Assess for malaria.
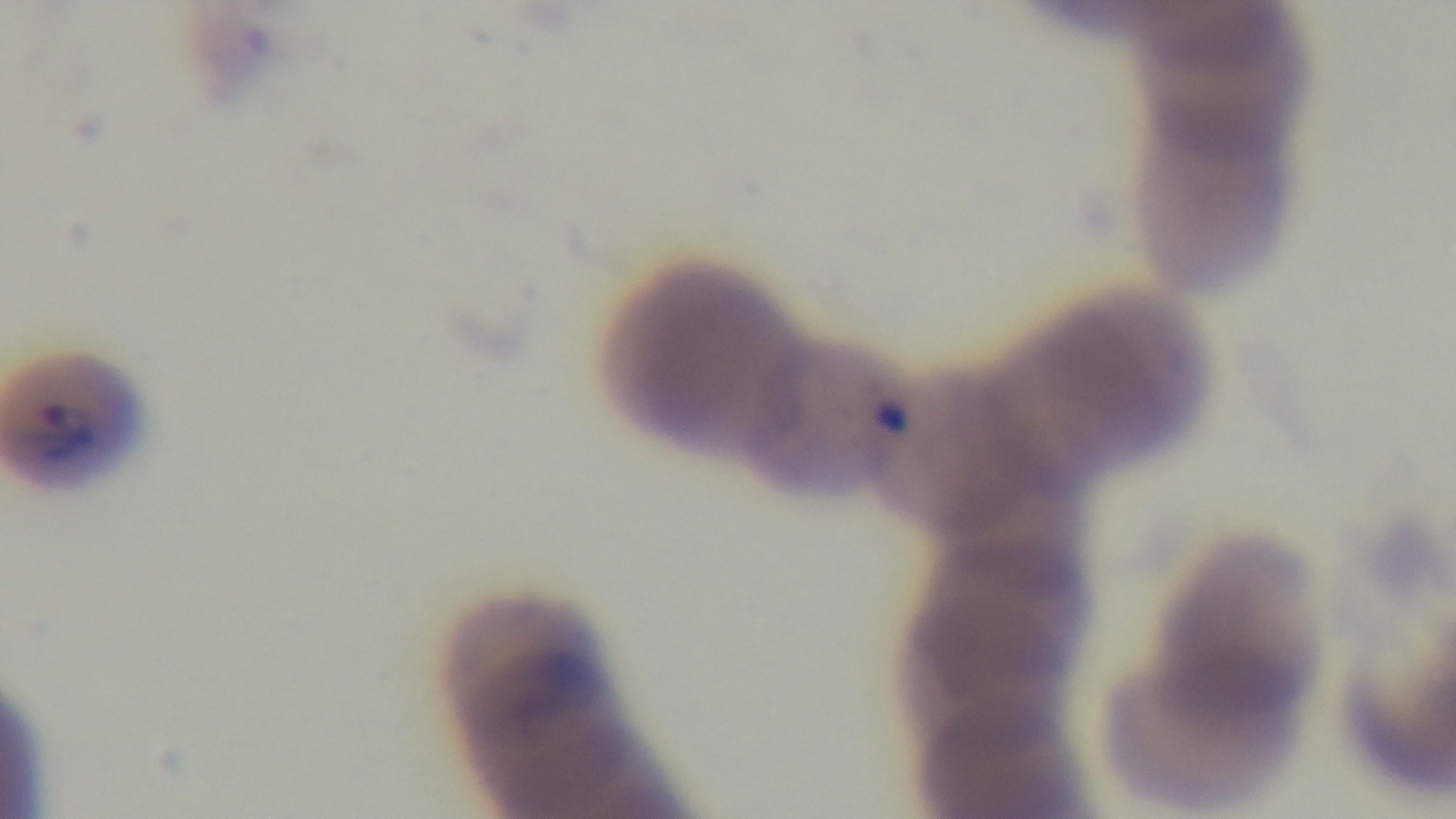

It is infected.

Preparation: thin blood film. One field from the slide. Light microscopy. 100x oil-immersion objective. Giemsa stain. Captured with a mounted 4K digital camera.